Assess this cell for malaria.
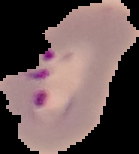

Parasitized.

image_type: cell region segmented out of the field of view; surrounding area masked to black
image_size: 139×154 pixels
preparation: thin blood smear